State which parasite is depicted.
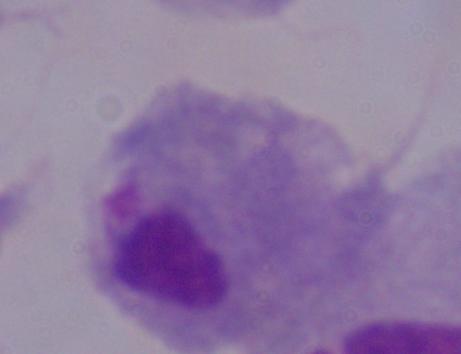
A trichomonad.

Captured at 1000x magnification. Micrograph.